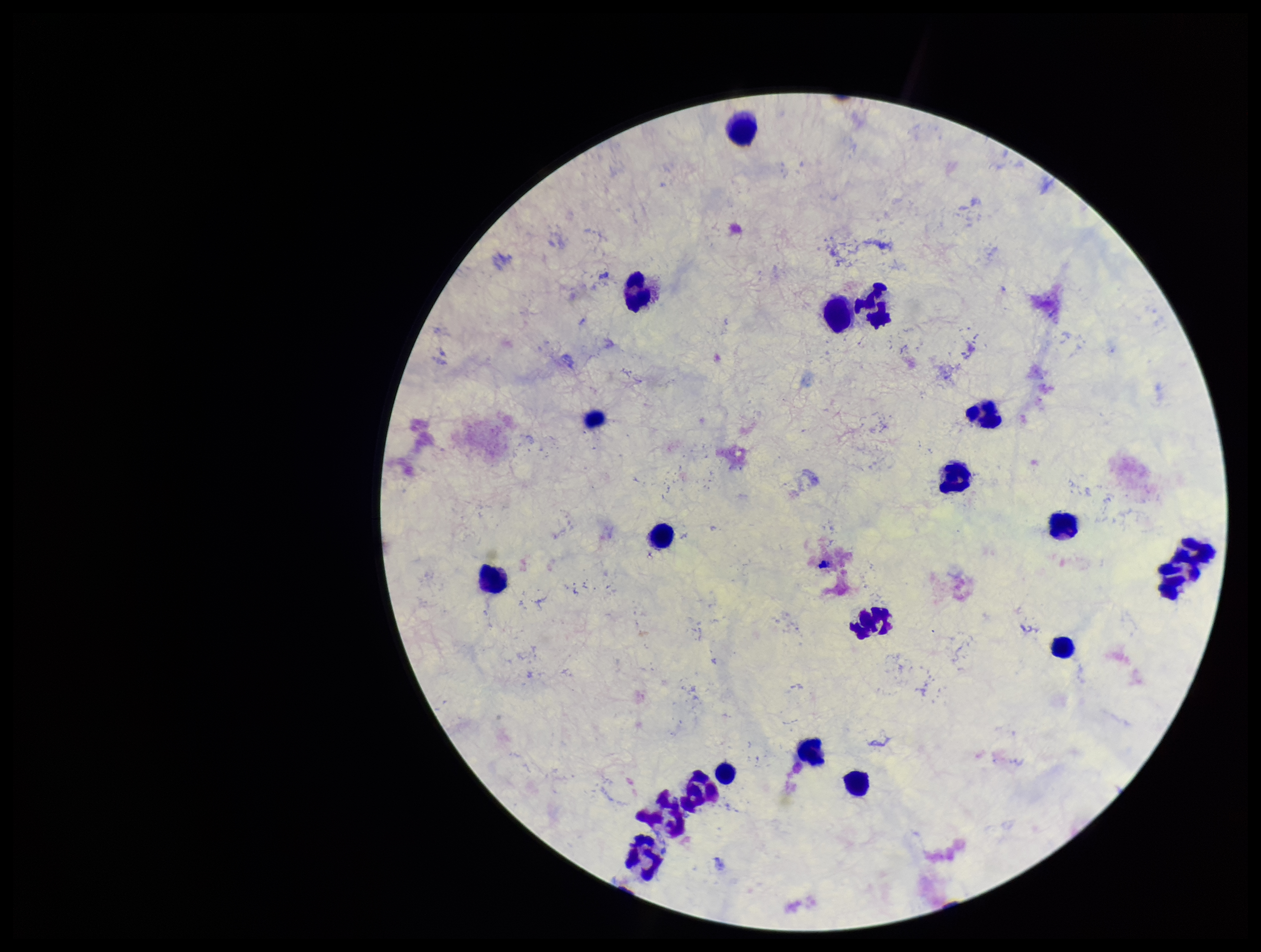

Summary:
  - Plasmodium parasites: none identified
  - Parasite count: 0
  - Capture: smartphone photograph through the microscope eyepiece
  - Leukocyte count: 20
  - Patient malaria status: negative
  - Stain: Giemsa
  - Image size: 1261×952 pixels
  - Field of view: single
  - Preparation: thick smear